Comment on the morphology of the erythrocytes.
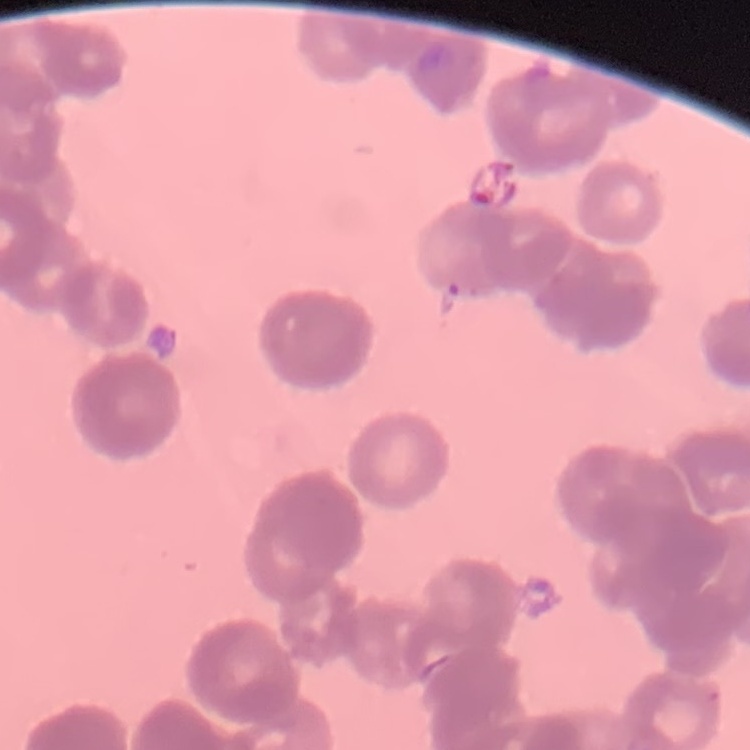
They show rouleaux formation.

Summary:
  - Preparation: thin peripheral smear
  - Image type: one tile cut from a larger photomicrograph
  - Stain: Field's or Giemsa